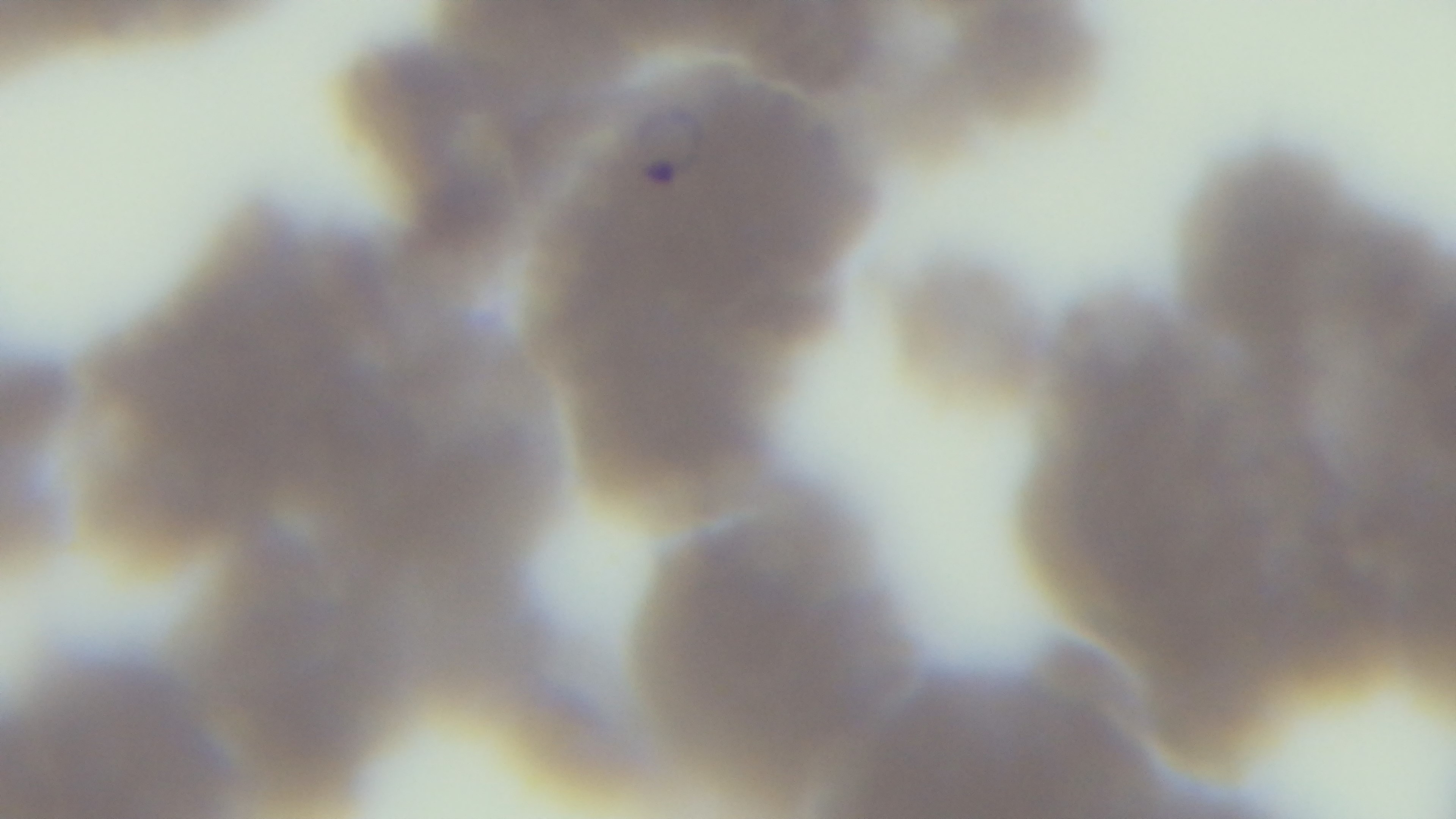

objective = 100x oil immersion
field of view = one from the slide
capture = mounted 4K digital camera
stain = Giemsa
malaria status = positive
modality = light microscopy
preparation = thin blood film